Assess for malaria.
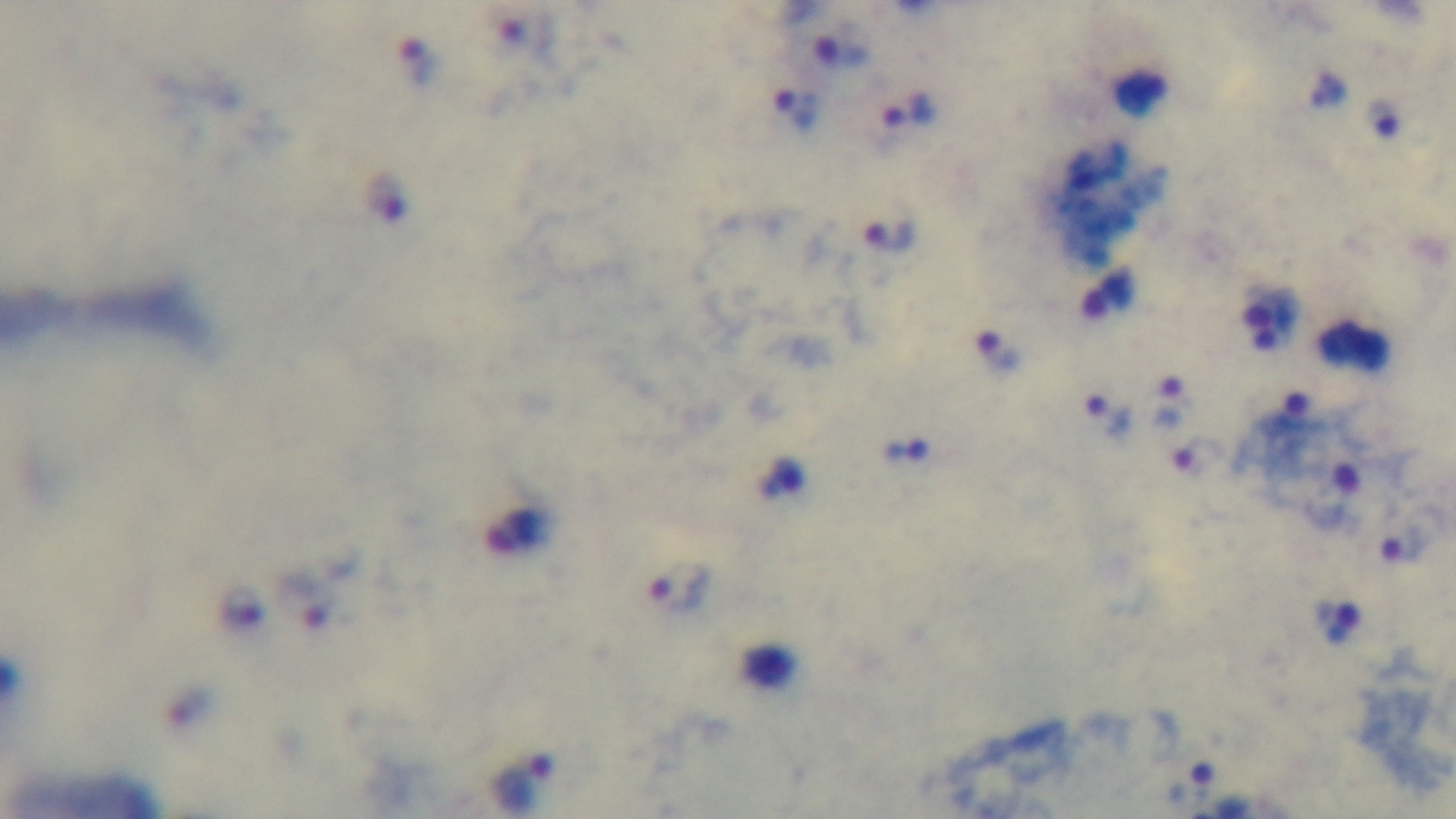
It is infected.

preparation: thick
objective: 100x oil immersion
field_of_view: one from the slide
stain: Giemsa
capture: mounted 4K digital camera
modality: light microscopy